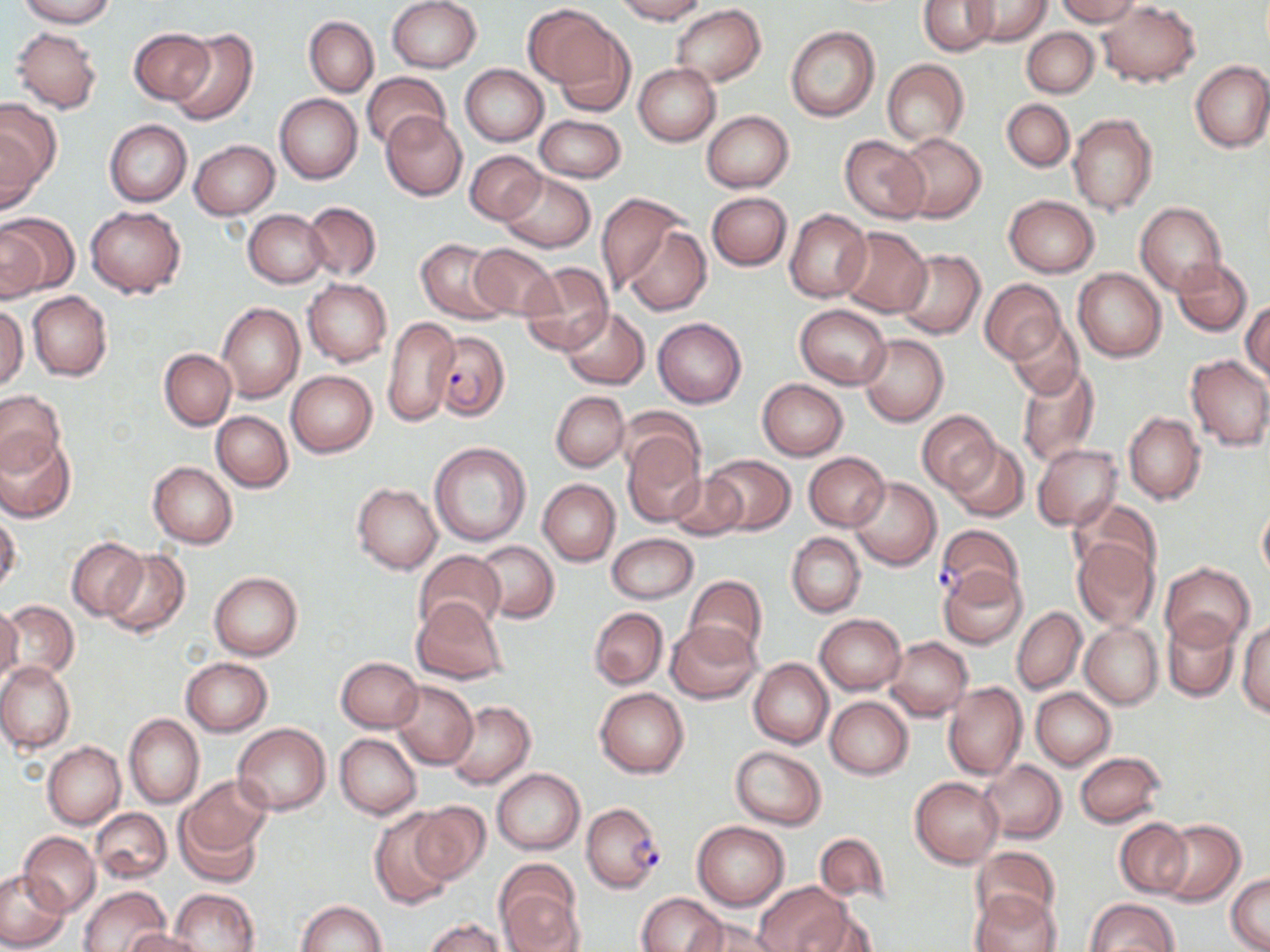
Summary:
  - Coordinate format: approximate bounding boxes as named x1/y1/x2/y2 corners in pixels
  - Uninfected red blood cell locations: (x1=17, y1=0, x2=115, y2=28), (x1=386, y1=0, x2=482, y2=73), (x1=614, y1=0, x2=708, y2=24), (x1=919, y1=0, x2=997, y2=54), (x1=964, y1=0, x2=1051, y2=46), (x1=1055, y1=0, x2=1140, y2=25), (x1=1097, y1=2, x2=1201, y2=85), (x1=672, y1=4, x2=766, y2=87), (x1=523, y1=5, x2=615, y2=87), (x1=304, y1=16, x2=379, y2=96), (x1=548, y1=19, x2=636, y2=114), (x1=785, y1=24, x2=880, y2=122), (x1=11, y1=26, x2=103, y2=112), (x1=130, y1=27, x2=212, y2=102), (x1=167, y1=27, x2=257, y2=126), (x1=1022, y1=28, x2=1099, y2=96), (x1=882, y1=59, x2=968, y2=147), (x1=1190, y1=60, x2=1270, y2=153), (x1=633, y1=63, x2=721, y2=145), (x1=460, y1=65, x2=548, y2=146), (x1=361, y1=72, x2=451, y2=152), (x1=275, y1=93, x2=362, y2=185), (x1=1001, y1=99, x2=1074, y2=171), (x1=0, y1=104, x2=58, y2=209), (x1=702, y1=111, x2=794, y2=193), (x1=381, y1=112, x2=466, y2=200), (x1=1069, y1=112, x2=1158, y2=215), (x1=535, y1=114, x2=626, y2=182), (x1=104, y1=120, x2=191, y2=206), (x1=896, y1=132, x2=986, y2=224), (x1=840, y1=135, x2=929, y2=223), (x1=189, y1=140, x2=279, y2=219), (x1=466, y1=150, x2=546, y2=224), (x1=497, y1=171, x2=596, y2=252), (x1=706, y1=191, x2=791, y2=270), (x1=598, y1=193, x2=693, y2=303), (x1=1004, y1=194, x2=1099, y2=278), (x1=303, y1=201, x2=381, y2=280), (x1=1136, y1=203, x2=1226, y2=295), (x1=84, y1=206, x2=185, y2=297), (x1=244, y1=210, x2=328, y2=287), (x1=784, y1=210, x2=871, y2=302), (x1=0, y1=213, x2=77, y2=297), (x1=622, y1=224, x2=712, y2=317), (x1=837, y1=227, x2=932, y2=317), (x1=416, y1=239, x2=508, y2=324), (x1=467, y1=242, x2=559, y2=321), (x1=895, y1=248, x2=985, y2=339), (x1=1172, y1=258, x2=1252, y2=336), (x1=519, y1=263, x2=613, y2=354), (x1=1073, y1=268, x2=1166, y2=362), (x1=303, y1=278, x2=391, y2=366), (x1=981, y1=279, x2=1064, y2=365), (x1=27, y1=292, x2=112, y2=382), (x1=1242, y1=302, x2=1269, y2=384), (x1=0, y1=303, x2=28, y2=389), (x1=217, y1=303, x2=305, y2=404), (x1=795, y1=304, x2=891, y2=389), (x1=560, y1=306, x2=651, y2=390), (x1=382, y1=315, x2=459, y2=425), (x1=653, y1=317, x2=746, y2=407), (x1=1004, y1=317, x2=1086, y2=401), (x1=859, y1=334, x2=949, y2=425), (x1=159, y1=348, x2=235, y2=430), (x1=1185, y1=353, x2=1270, y2=451), (x1=1016, y1=364, x2=1100, y2=467), (x1=287, y1=370, x2=377, y2=456), (x1=756, y1=378, x2=849, y2=460), (x1=0, y1=390, x2=65, y2=474), (x1=551, y1=391, x2=629, y2=471), (x1=618, y1=407, x2=703, y2=488), (x1=918, y1=409, x2=998, y2=493), (x1=1123, y1=410, x2=1206, y2=505), (x1=212, y1=411, x2=292, y2=492), (x1=623, y1=433, x2=706, y2=526), (x1=1, y1=434, x2=75, y2=522), (x1=946, y1=438, x2=1028, y2=522), (x1=429, y1=442, x2=531, y2=546), (x1=1032, y1=443, x2=1122, y2=532), (x1=803, y1=452, x2=890, y2=532), (x1=704, y1=454, x2=793, y2=535), (x1=149, y1=461, x2=238, y2=548), (x1=666, y1=471, x2=748, y2=541), (x1=850, y1=477, x2=940, y2=569), (x1=538, y1=479, x2=620, y2=565), (x1=353, y1=483, x2=442, y2=574), (x1=1072, y1=498, x2=1163, y2=581), (x1=1257, y1=499, x2=1270, y2=585), (x1=0, y1=513, x2=21, y2=594), (x1=787, y1=532, x2=865, y2=618), (x1=607, y1=533, x2=698, y2=603), (x1=67, y1=537, x2=146, y2=621), (x1=1071, y1=538, x2=1159, y2=631), (x1=475, y1=541, x2=559, y2=623), (x1=104, y1=549, x2=189, y2=637), (x1=412, y1=550, x2=506, y2=637), (x1=1161, y1=563, x2=1254, y2=647), (x1=938, y1=566, x2=1029, y2=649), (x1=209, y1=571, x2=303, y2=659), (x1=685, y1=576, x2=768, y2=659), (x1=411, y1=598, x2=507, y2=684), (x1=3, y1=600, x2=80, y2=681), (x1=0, y1=605, x2=21, y2=688), (x1=590, y1=607, x2=668, y2=688), (x1=1012, y1=607, x2=1085, y2=694), (x1=1162, y1=613, x2=1240, y2=702), (x1=815, y1=614, x2=906, y2=695), (x1=665, y1=620, x2=759, y2=704), (x1=1238, y1=620, x2=1270, y2=718), (x1=1079, y1=621, x2=1162, y2=708), (x1=885, y1=637, x2=973, y2=720), (x1=181, y1=657, x2=272, y2=735), (x1=336, y1=657, x2=423, y2=732), (x1=748, y1=657, x2=833, y2=749), (x1=0, y1=662, x2=75, y2=753), (x1=390, y1=680, x2=478, y2=769), (x1=942, y1=681, x2=1028, y2=779), (x1=595, y1=687, x2=688, y2=777), (x1=1030, y1=688, x2=1116, y2=770), (x1=825, y1=696, x2=913, y2=779), (x1=446, y1=701, x2=535, y2=789), (x1=124, y1=714, x2=204, y2=809), (x1=233, y1=722, x2=330, y2=814), (x1=336, y1=733, x2=422, y2=819), (x1=44, y1=742, x2=124, y2=828), (x1=730, y1=746, x2=827, y2=829), (x1=1075, y1=752, x2=1165, y2=828), (x1=979, y1=760, x2=1066, y2=844), (x1=492, y1=769, x2=585, y2=854), (x1=178, y1=776, x2=272, y2=862), (x1=910, y1=777, x2=1004, y2=868), (x1=410, y1=801, x2=489, y2=885), (x1=91, y1=808, x2=171, y2=883), (x1=370, y1=810, x2=457, y2=909), (x1=1115, y1=818, x2=1193, y2=898), (x1=1153, y1=819, x2=1245, y2=907), (x1=691, y1=820, x2=789, y2=910), (x1=19, y1=833, x2=100, y2=917), (x1=814, y1=833, x2=892, y2=908), (x1=971, y1=846, x2=1061, y2=930), (x1=496, y1=865, x2=582, y2=949), (x1=0, y1=871, x2=69, y2=950), (x1=1227, y1=874, x2=1270, y2=952), (x1=755, y1=881, x2=851, y2=952), (x1=78, y1=886, x2=169, y2=952), (x1=169, y1=888, x2=258, y2=952), (x1=971, y1=890, x2=1062, y2=952), (x1=637, y1=893, x2=726, y2=952), (x1=1084, y1=898, x2=1178, y2=952), (x1=296, y1=901, x2=388, y2=952), (x1=796, y1=907, x2=880, y2=952), (x1=690, y1=916, x2=783, y2=952), (x1=425, y1=919, x2=505, y2=952), (x1=125, y1=929, x2=210, y2=952)
  - Plasmodium falciparum-infected red blood cell locations: (x1=430, y1=332, x2=509, y2=420), (x1=936, y1=524, x2=1025, y2=602), (x1=582, y1=802, x2=666, y2=892)
  - Slide-level diagnosis: Plasmodium falciparum
  - Magnification: 1000x
  - Modality: optical microscopy
  - Preparation: thin blood film
  - Image size: 1270×952 pixels
  - Field of view: one of a larger specimen
  - Stain: May-Grünwald-Giemsa